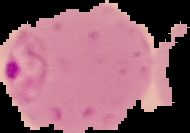
Summary:
  - Result: Plasmodium parasites detected
  - Image size: 190×133 pixels
  - Image type: segmented cell region on a black background
  - Preparation: thin blood smear